Assess this cell for malaria.
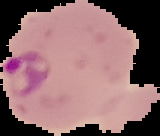

It is parasitized.

Summary:
  - Image size: 160×136 pixels
  - Preparation: thin blood film
  - Image type: segmented cell region on a black background